Assess this cell for malaria.
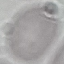
Uninfected.

stain = Giemsa
image type = cell patch, automatically extracted from a larger field of view and resized to 64 × 64 pixels
capture = smartphone through the microscope eyepiece
preparation = thin blood film